Outline platelets.
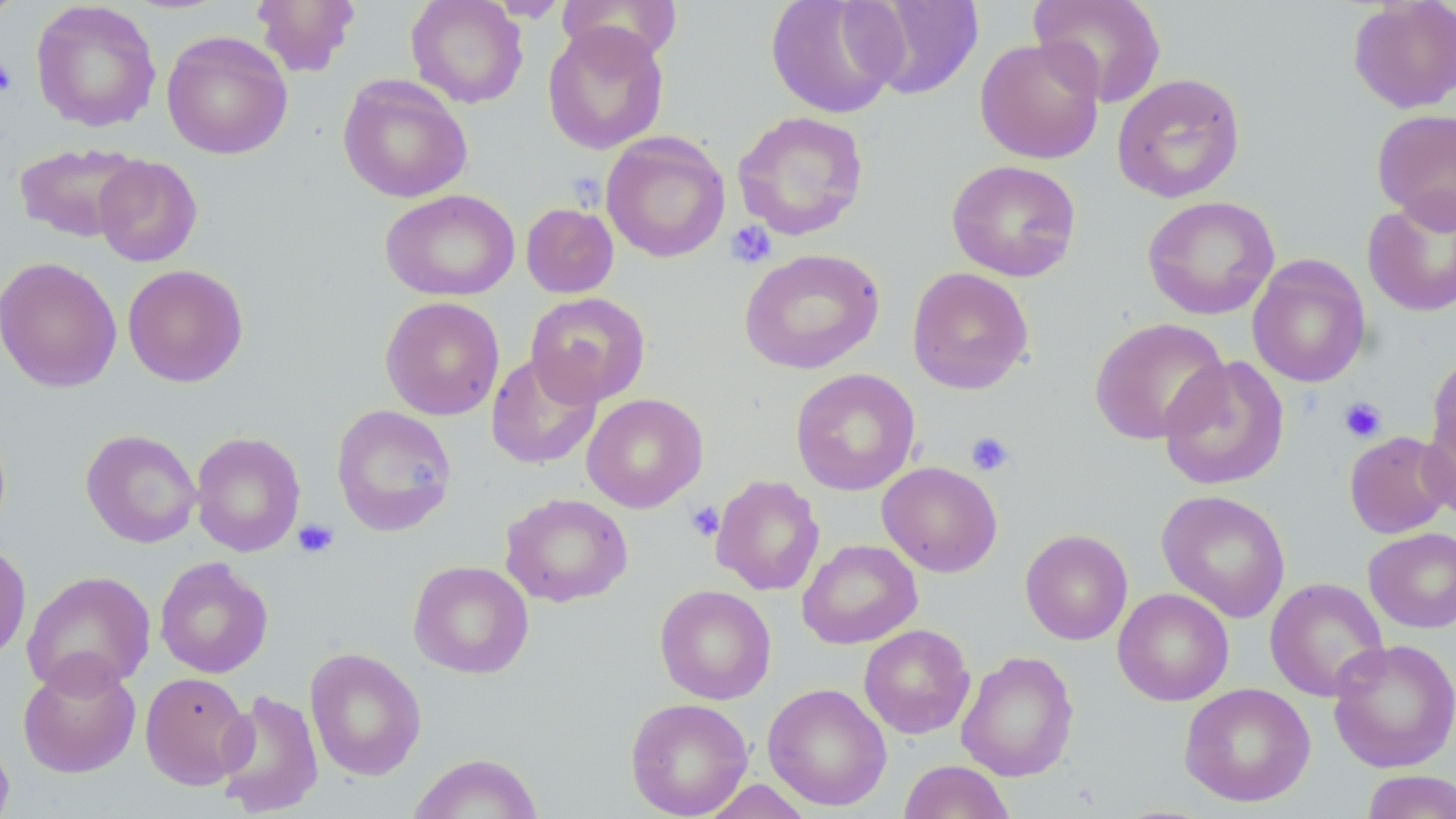

Approximate bounding boxes as named x1/y1/x2/y2 corners in pixels.
Platelets: (x1=0, y1=57, x2=17, y2=97), (x1=568, y1=171, x2=606, y2=209), (x1=725, y1=220, x2=778, y2=269), (x1=1338, y1=396, x2=1388, y2=443), (x1=965, y1=431, x2=1015, y2=476), (x1=684, y1=500, x2=724, y2=541), (x1=293, y1=518, x2=340, y2=559).

Uninfected red blood cell locations: (x1=0, y1=0, x2=23, y2=26), (x1=250, y1=0, x2=360, y2=77), (x1=406, y1=0, x2=528, y2=108), (x1=557, y1=0, x2=683, y2=67), (x1=765, y1=0, x2=904, y2=119), (x1=1029, y1=0, x2=1167, y2=108), (x1=1347, y1=0, x2=1456, y2=113), (x1=854, y1=1, x2=985, y2=100), (x1=31, y1=2, x2=161, y2=133), (x1=542, y1=23, x2=669, y2=154), (x1=162, y1=30, x2=292, y2=159), (x1=975, y1=36, x2=1105, y2=164), (x1=1112, y1=72, x2=1246, y2=202), (x1=338, y1=74, x2=472, y2=203), (x1=1372, y1=109, x2=1456, y2=231), (x1=732, y1=110, x2=869, y2=241), (x1=601, y1=132, x2=730, y2=262), (x1=14, y1=142, x2=144, y2=243), (x1=93, y1=155, x2=202, y2=267), (x1=946, y1=159, x2=1082, y2=282), (x1=380, y1=189, x2=520, y2=301), (x1=1362, y1=193, x2=1456, y2=317), (x1=1142, y1=195, x2=1280, y2=319), (x1=521, y1=202, x2=618, y2=298), (x1=739, y1=248, x2=886, y2=375), (x1=1248, y1=255, x2=1370, y2=388), (x1=0, y1=257, x2=122, y2=392), (x1=123, y1=264, x2=248, y2=387), (x1=907, y1=266, x2=1034, y2=395), (x1=525, y1=292, x2=650, y2=407), (x1=380, y1=296, x2=505, y2=420), (x1=1090, y1=317, x2=1230, y2=445), (x1=486, y1=352, x2=602, y2=470), (x1=1425, y1=352, x2=1456, y2=477), (x1=1158, y1=355, x2=1289, y2=491), (x1=790, y1=368, x2=920, y2=496), (x1=582, y1=393, x2=708, y2=513), (x1=1419, y1=399, x2=1456, y2=523), (x1=331, y1=404, x2=457, y2=536), (x1=81, y1=429, x2=201, y2=548), (x1=191, y1=431, x2=305, y2=556), (x1=1343, y1=431, x2=1454, y2=539), (x1=877, y1=461, x2=1002, y2=577), (x1=710, y1=474, x2=825, y2=596), (x1=1157, y1=490, x2=1291, y2=623), (x1=500, y1=492, x2=633, y2=608), (x1=1364, y1=527, x2=1456, y2=633), (x1=1020, y1=529, x2=1133, y2=645), (x1=797, y1=539, x2=922, y2=649), (x1=0, y1=541, x2=31, y2=664), (x1=154, y1=557, x2=273, y2=678), (x1=408, y1=560, x2=534, y2=679), (x1=22, y1=570, x2=156, y2=696), (x1=1265, y1=577, x2=1389, y2=701), (x1=655, y1=584, x2=776, y2=704), (x1=1113, y1=588, x2=1234, y2=706), (x1=859, y1=624, x2=975, y2=739), (x1=1327, y1=638, x2=1456, y2=773), (x1=304, y1=647, x2=427, y2=781), (x1=956, y1=651, x2=1079, y2=782), (x1=17, y1=655, x2=141, y2=778), (x1=139, y1=671, x2=253, y2=790), (x1=763, y1=683, x2=892, y2=811), (x1=1179, y1=683, x2=1316, y2=807), (x1=215, y1=689, x2=324, y2=817), (x1=625, y1=697, x2=753, y2=818), (x1=0, y1=730, x2=14, y2=819), (x1=407, y1=752, x2=543, y2=818), (x1=898, y1=759, x2=1016, y2=819), (x1=1359, y1=769, x2=1456, y2=819), (x1=698, y1=779, x2=816, y2=818). Slide-level diagnosis: negative for blood parasites. Image is 1456×819 pixels. Light microscopy. Captured at 1000x magnification. May-Grünwald-Giemsa stain. Thin blood smear. Single field of view.